Name the parasite shown.
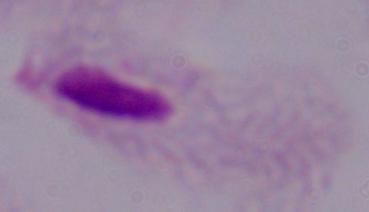
A trichomonad.

modality = photomicrograph
magnification = 1000x